Give the extent of all uninfected red blood cells.
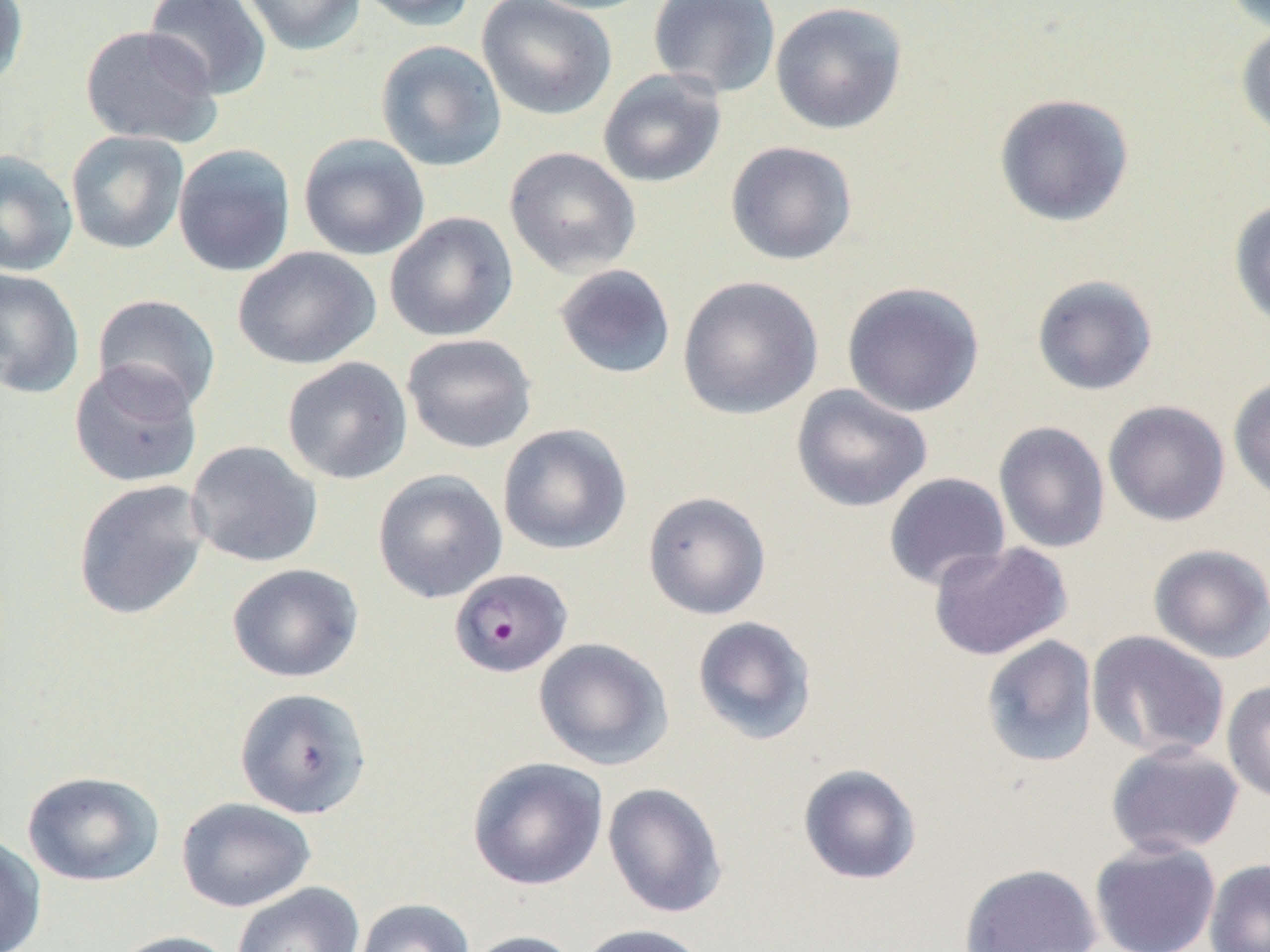

Approximate bounding boxes as [x1, y1, x2, y2] in pixels.
Uninfected red blood cells (subset): [0, 0, 29, 90], [144, 0, 272, 100], [239, 0, 366, 56], [354, 0, 479, 32], [476, 0, 617, 121], [522, 0, 658, 15], [647, 0, 781, 99], [1223, 1, 1270, 34], [770, 2, 908, 135], [1235, 22, 1270, 145], [79, 25, 222, 148], [375, 40, 507, 172], [597, 69, 727, 188], [993, 93, 1135, 227], [65, 130, 189, 254], [298, 133, 430, 261], [725, 141, 858, 266], [172, 143, 296, 277], [504, 146, 642, 278], [0, 150, 79, 277], [1229, 198, 1270, 334], [384, 212, 518, 342], [233, 246, 380, 370], [553, 264, 677, 380], [0, 268, 85, 399], [1031, 274, 1159, 396], [677, 275, 823, 421], [841, 281, 985, 418], [91, 294, 222, 414], [401, 333, 538, 454], [282, 357, 413, 485], [68, 359, 203, 489], [1228, 374, 1270, 503], [791, 384, 933, 513], [1103, 400, 1230, 526], [993, 421, 1111, 553], [498, 424, 632, 555], [185, 440, 323, 568], [372, 469, 507, 604], [883, 472, 1010, 591], [73, 479, 210, 621], [643, 491, 771, 620], [927, 541, 1073, 660], [1148, 543, 1270, 663], [226, 563, 363, 683], [692, 616, 817, 745], [1087, 630, 1230, 760], [980, 635, 1099, 769], [533, 637, 673, 770], [1222, 679, 1270, 804], [234, 687, 372, 819], [1105, 742, 1245, 858], [466, 756, 609, 891], [798, 763, 922, 885], [21, 770, 165, 887], [602, 782, 728, 918], [176, 797, 316, 912], [0, 832, 47, 952], [1089, 839, 1222, 952], [1204, 857, 1270, 952], [959, 862, 1102, 952], [232, 882, 365, 952], [355, 898, 475, 952], [578, 923, 709, 952], [107, 930, 239, 952], [462, 930, 584, 952].

Slide-level diagnosis: Plasmodium falciparum. Light microscopy. Thin blood smear. Single field of view. 1000x magnification. Image is 1270×952 pixels.